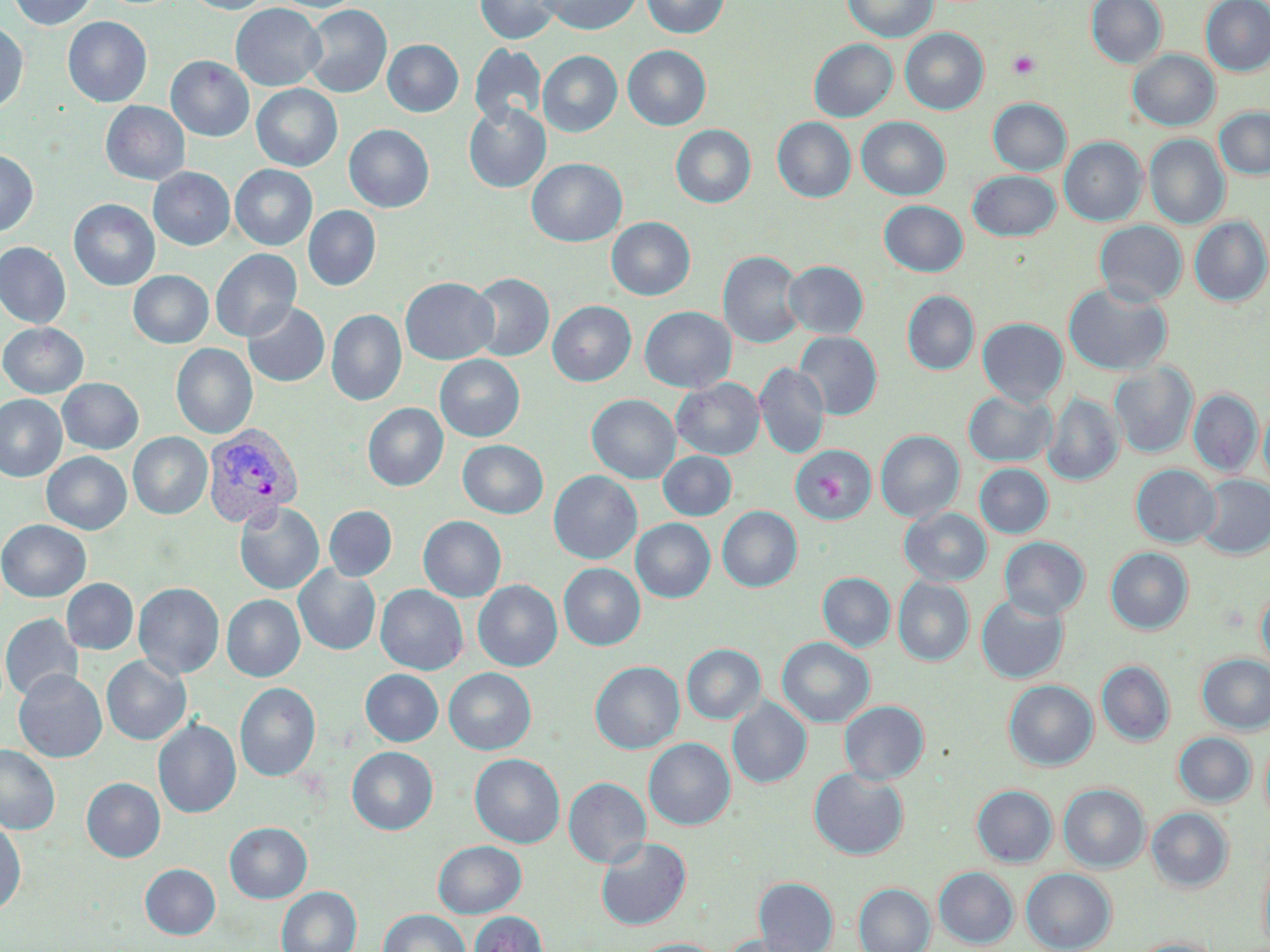
Approximate bounding boxes as (x1, y1, x2, y2) in pixels. Uninfected red blood cell locations: (8, 0, 97, 29), (185, 0, 273, 14), (272, 0, 363, 13), (475, 0, 562, 44), (540, 0, 642, 35), (641, 0, 729, 38), (842, 0, 937, 42), (1086, 0, 1167, 68), (1201, 0, 1270, 76), (231, 3, 326, 91), (302, 4, 392, 98), (62, 17, 152, 107), (0, 22, 28, 114), (900, 28, 989, 114), (383, 39, 463, 116), (809, 39, 897, 122), (469, 44, 546, 128), (623, 45, 711, 130), (538, 50, 622, 137), (1128, 50, 1220, 131), (166, 56, 254, 141), (251, 84, 343, 171), (988, 98, 1071, 175), (100, 101, 190, 185), (463, 102, 551, 193), (1214, 107, 1270, 179), (856, 117, 950, 200), (773, 118, 856, 202), (344, 124, 434, 212), (671, 125, 756, 208), (1144, 134, 1230, 229), (1060, 137, 1147, 226), (0, 149, 38, 237), (526, 158, 627, 247), (230, 165, 317, 250), (148, 167, 234, 250), (968, 170, 1061, 241), (69, 199, 160, 290), (879, 200, 967, 276), (304, 205, 381, 290), (1189, 216, 1270, 306), (606, 217, 695, 300), (1094, 220, 1187, 305), (0, 241, 71, 328), (210, 248, 302, 341), (718, 251, 806, 348), (784, 261, 868, 338), (128, 270, 213, 348), (467, 272, 554, 361), (400, 277, 499, 365), (1063, 282, 1172, 376), (902, 290, 979, 375), (548, 300, 636, 386), (242, 301, 330, 387), (640, 306, 736, 393), (326, 309, 406, 406), (977, 317, 1068, 406), (0, 322, 88, 398), (794, 331, 882, 419), (171, 343, 257, 439), (435, 354, 525, 441), (1109, 362, 1198, 458), (754, 363, 830, 459), (57, 378, 144, 454), (671, 378, 765, 459), (1188, 389, 1262, 477), (963, 390, 1056, 466), (1044, 393, 1124, 486), (0, 394, 67, 481), (587, 394, 680, 483), (363, 403, 448, 491), (1259, 405, 1270, 490), (875, 430, 964, 522), (128, 432, 212, 519), (457, 440, 548, 518), (790, 442, 878, 522), (658, 451, 736, 520), (42, 452, 131, 534), (974, 463, 1053, 538), (1130, 464, 1220, 547), (549, 471, 642, 564), (1196, 475, 1270, 559), (234, 502, 324, 594), (324, 506, 397, 580), (717, 506, 802, 592), (900, 507, 992, 586), (418, 516, 506, 602), (631, 518, 715, 602), (0, 519, 91, 601), (999, 536, 1090, 620), (1105, 547, 1193, 634), (559, 563, 645, 650), (294, 566, 381, 655), (818, 572, 895, 652), (893, 577, 974, 666), (61, 578, 138, 654), (473, 580, 562, 671), (133, 582, 224, 679), (376, 585, 468, 675), (1257, 587, 1270, 671), (222, 594, 305, 681), (976, 594, 1069, 684), (1, 613, 83, 702), (776, 637, 875, 727), (682, 644, 765, 724), (1197, 654, 1270, 734), (101, 656, 191, 745), (1096, 660, 1175, 747), (590, 661, 685, 754), (444, 667, 536, 755), (361, 669, 443, 746), (14, 670, 107, 763), (1004, 679, 1098, 770), (235, 682, 321, 781), (727, 697, 812, 788), (839, 700, 929, 784), (154, 718, 241, 818), (1173, 732, 1256, 806), (1260, 733, 1270, 828), (644, 737, 735, 830), (0, 744, 60, 834), (347, 746, 438, 834), (469, 753, 565, 848), (808, 767, 909, 859), (563, 777, 651, 868), (82, 778, 165, 862), (1058, 783, 1149, 872), (972, 785, 1057, 867), (1146, 807, 1234, 893), (0, 820, 26, 914), (224, 822, 312, 903), (596, 836, 692, 929), (432, 840, 526, 917), (1259, 849, 1270, 949), (140, 864, 221, 939), (933, 866, 1019, 949), (1021, 868, 1116, 951), (754, 877, 839, 951), (853, 883, 936, 952), (276, 886, 362, 952), (379, 909, 470, 952), (468, 910, 548, 952), (721, 934, 814, 952), (1127, 937, 1223, 952), (631, 938, 723, 952). Platelet locations: (1007, 50, 1041, 79). Plasmodium vivax-infected red blood cell locations: (202, 424, 303, 529). Slide-level diagnosis: Plasmodium vivax. May-Grünwald-Giemsa-stained preparation. Light microscopy. Captured at 1000x magnification. Image is 1270×952 pixels. Thin blood film. One field of a larger specimen.